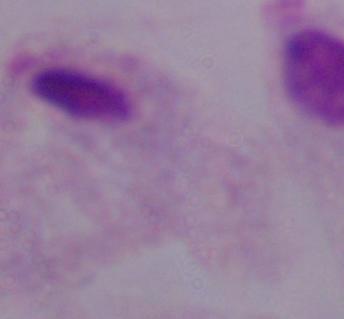

Summary:
  - Modality: micrograph
  - Magnification: 1000x
  - Identification: trichomonad